Point out every malaria parasite.
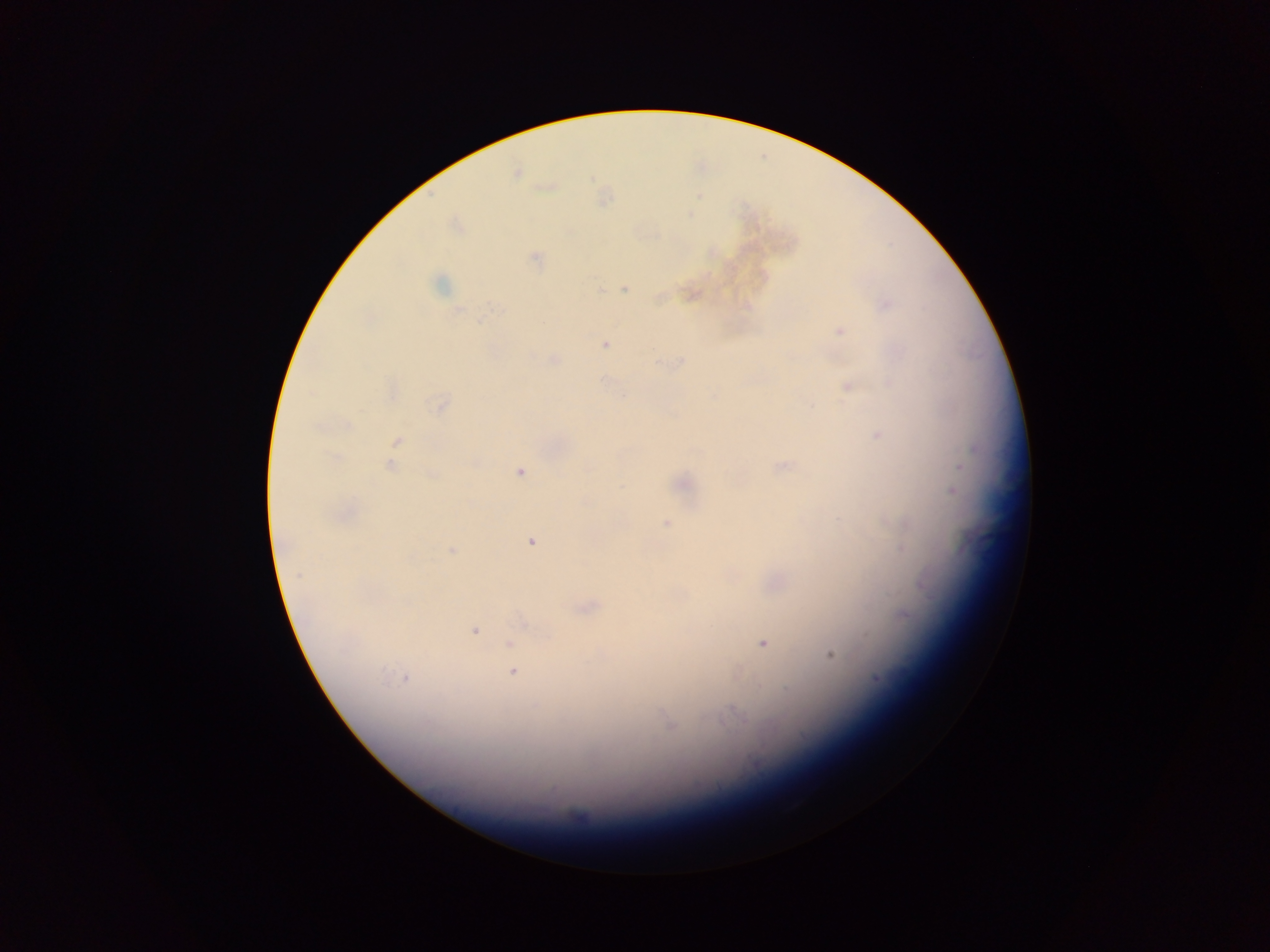
Approximate centers as [x, y] in pixels.
Malaria parasites: [517, 174], [536, 257], [439, 284], [624, 288], [598, 290], [887, 304], [458, 311], [839, 331], [605, 344], [554, 359], [679, 363], [847, 386], [622, 396], [440, 404], [348, 424], [877, 435], [397, 440], [334, 457], [390, 465], [783, 467], [959, 467], [519, 472], [432, 475], [953, 492], [667, 524], [531, 542], [902, 548], [452, 550], [299, 575], [926, 587], [904, 614], [475, 631], [509, 643], [763, 643], [830, 655], [512, 672], [407, 678], [877, 679], [736, 713], [670, 723], [757, 764].

Sample from Ghana. Thick blood film. Image is 1270×952 pixels. Mobile-phone photograph taken through the microscope. One field of view.